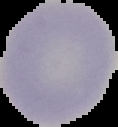

image type = segmented cell region with the area outside set to black
image size = 118×127 pixels
preparation = thin blood film
result = negative for malaria parasites